Locate every Plasmodium parasite.
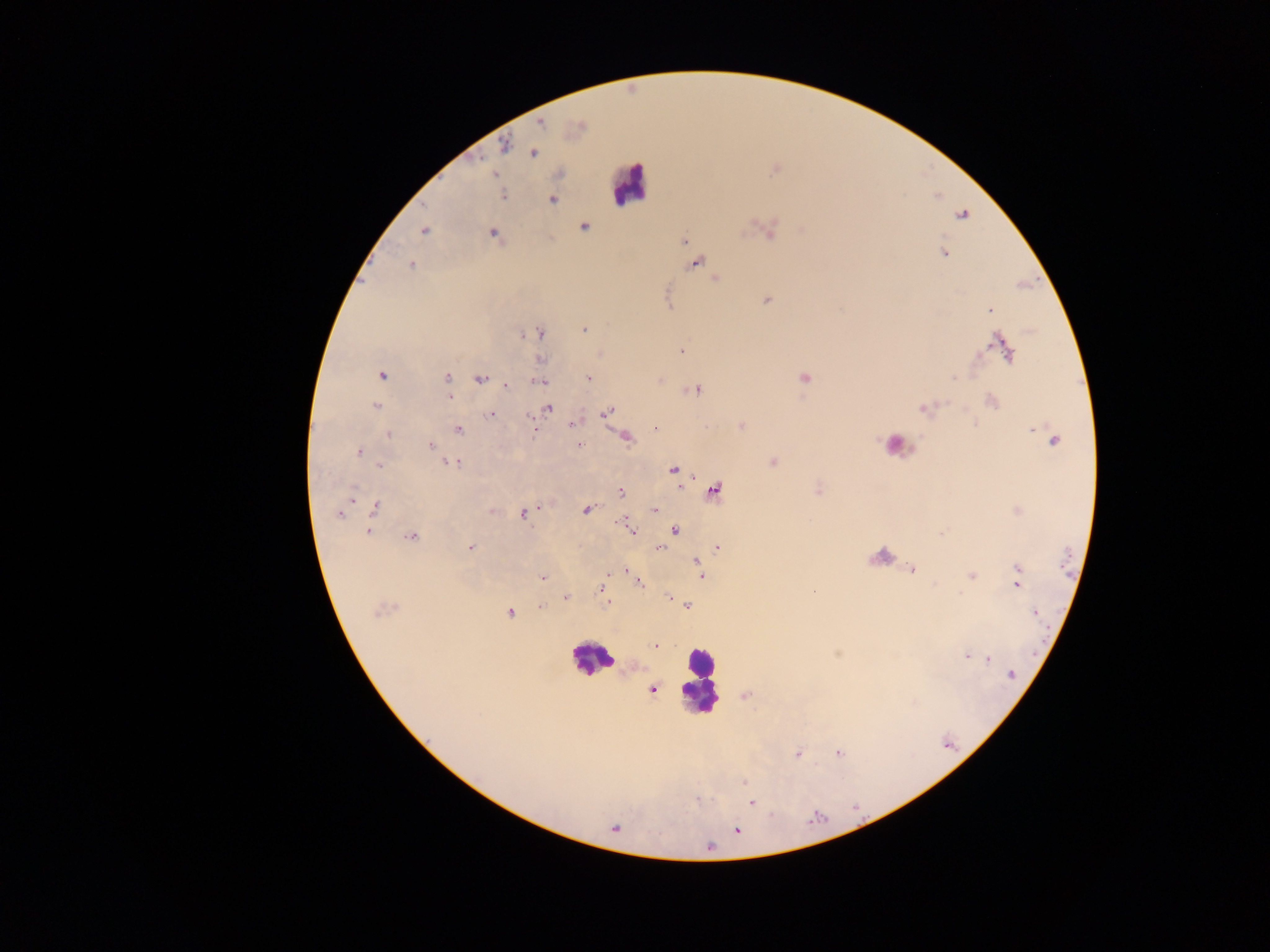

Approximate centers as (x, y) in pixels.
Plasmodium parasites: (540, 123), (580, 127), (504, 145), (533, 153), (494, 174), (503, 195), (552, 200), (962, 214), (584, 226), (769, 229), (424, 230), (802, 230), (492, 233), (684, 240), (944, 252), (695, 262), (410, 265), (715, 279), (766, 299), (989, 310), (583, 329), (539, 334), (1003, 347), (681, 351), (599, 354), (540, 359), (381, 374), (447, 377), (588, 377), (804, 378), (480, 379), (538, 381), (505, 384), (694, 389), (447, 397), (991, 401), (375, 407), (924, 407), (547, 408), (606, 412), (492, 414), (574, 423), (741, 425), (705, 427), (655, 428), (458, 429), (534, 430), (389, 434), (624, 436), (1053, 440), (579, 445), (431, 446), (359, 451), (774, 461), (452, 462), (380, 464), (673, 471), (713, 490), (818, 490), (621, 492), (375, 508), (586, 509), (654, 509), (491, 511), (1017, 511), (339, 512), (523, 513), (627, 526), (674, 530), (369, 531), (631, 531), (411, 537), (471, 548), (658, 548), (718, 548), (696, 560), (697, 567), (1019, 568), (911, 569), (625, 570), (971, 575), (701, 576), (542, 578), (639, 582), (1016, 583), (602, 587), (813, 590), (566, 597), (668, 597), (607, 602), (687, 606), (540, 607), (382, 609), (509, 612), (1034, 613), (654, 645), (967, 655), (987, 659), (1011, 673), (651, 688), (746, 694), (838, 753), (797, 754), (742, 781), (751, 802), (615, 827), (736, 830).

Summary:
  - Leukocyte locations: (628, 184), (896, 445), (879, 557), (591, 659), (700, 682)
  - Capture: mobile-phone photograph through a microscope
  - Field of view: single
  - Preparation: thick blood film
  - Image size: 1270×952 pixels
  - Country: Ghana